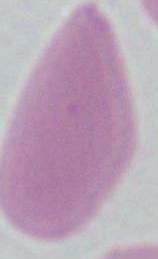

Summary:
  - Modality: photomicrograph
  - Magnification: 1000x
  - Identification: erythrocyte